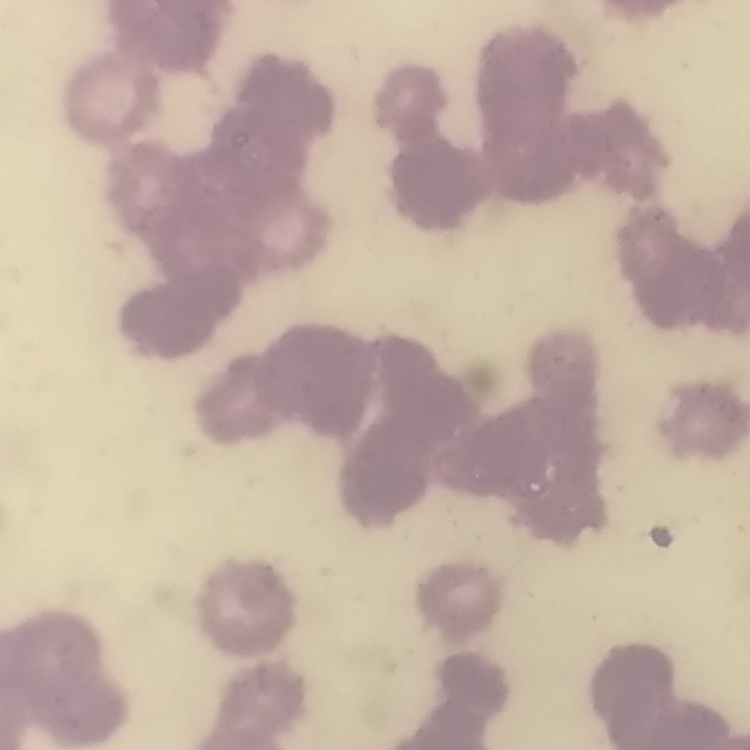
Summary:
  - Red blood cell morphology: rouleaux formation
  - Image type: square crop of a larger photomicrograph
  - Stain: Field's or Giemsa
  - Preparation: thin peripheral smear